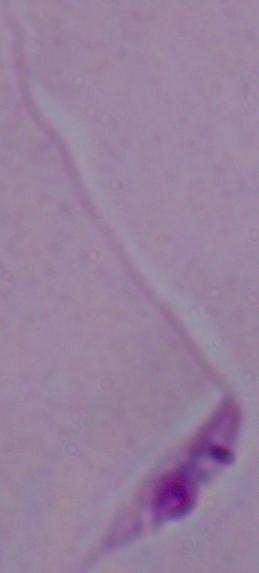

modality: photomicrograph
identification: Leishmania
magnification: 1000x